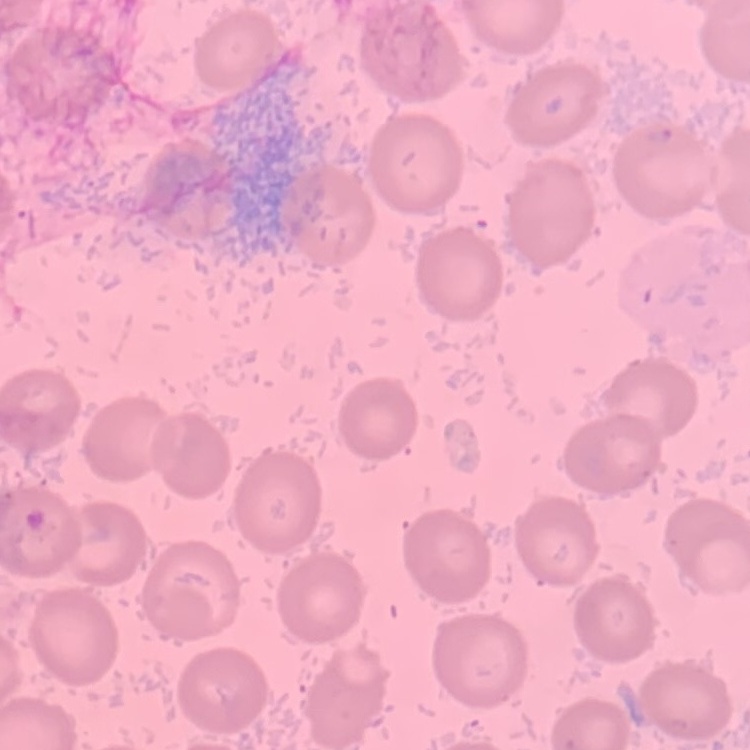

The erythrocytes exhibit no rouleaux formation. Thin blood smear. One tile cut from a larger photomicrograph. Stained with either Field's or Giemsa.